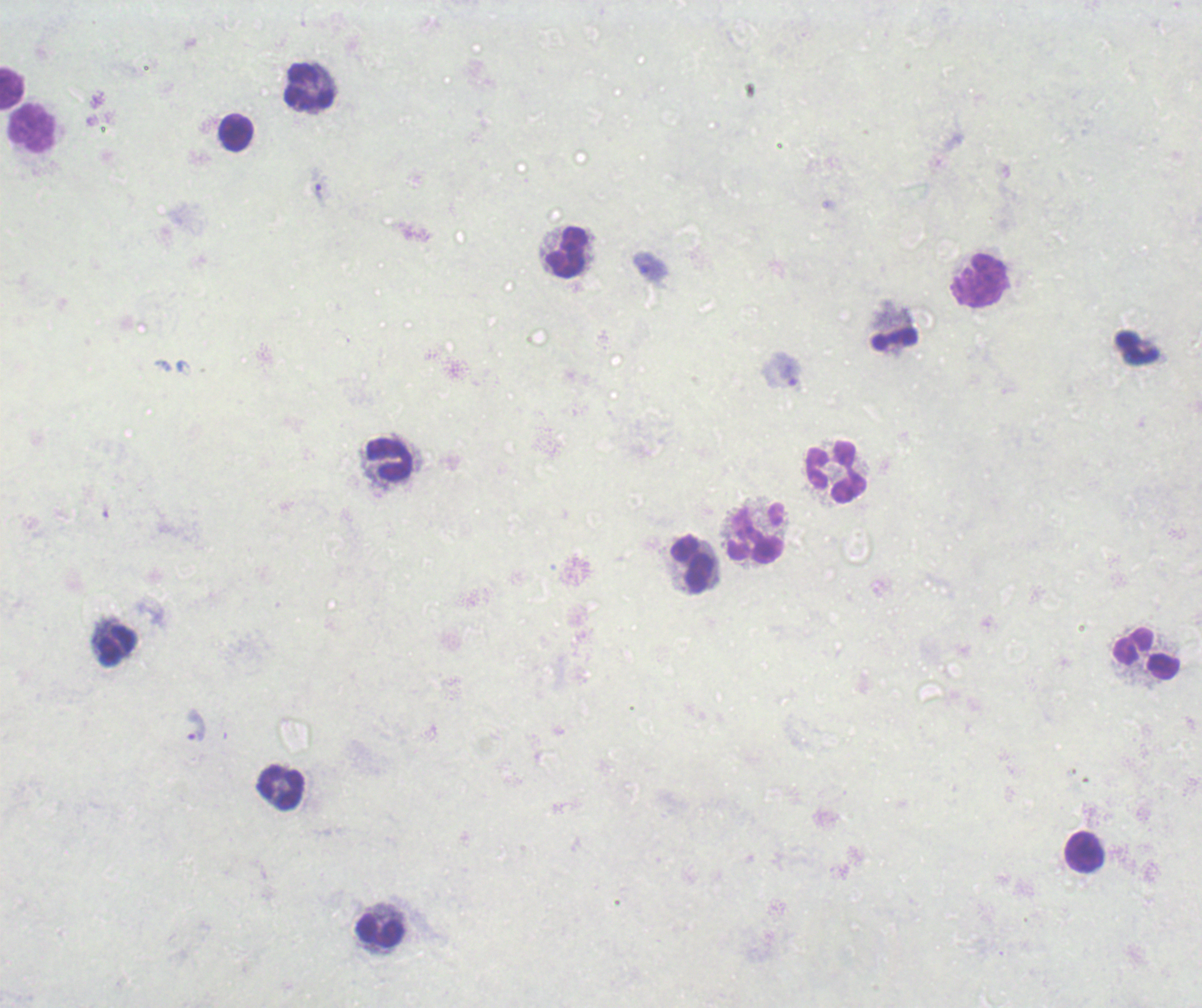
Approximate object centers, in pixels from the top-left corner. Leukocyte locations: (x=11, y=87), (x=309, y=87), (x=33, y=129), (x=237, y=133), (x=567, y=253), (x=979, y=280), (x=391, y=459), (x=836, y=472), (x=755, y=534), (x=693, y=563), (x=117, y=647), (x=1146, y=654), (x=281, y=788), (x=1084, y=852), (x=381, y=932). Trophozoite locations: (x=320, y=192), (x=650, y=267), (x=195, y=727). 100x magnification. Romanowsky stain. Result: malaria parasites identified. Single field of view. Thick blood film. Background quality: poor. Previously used in an actual diagnosis. Image is 1202×1008 pixels.